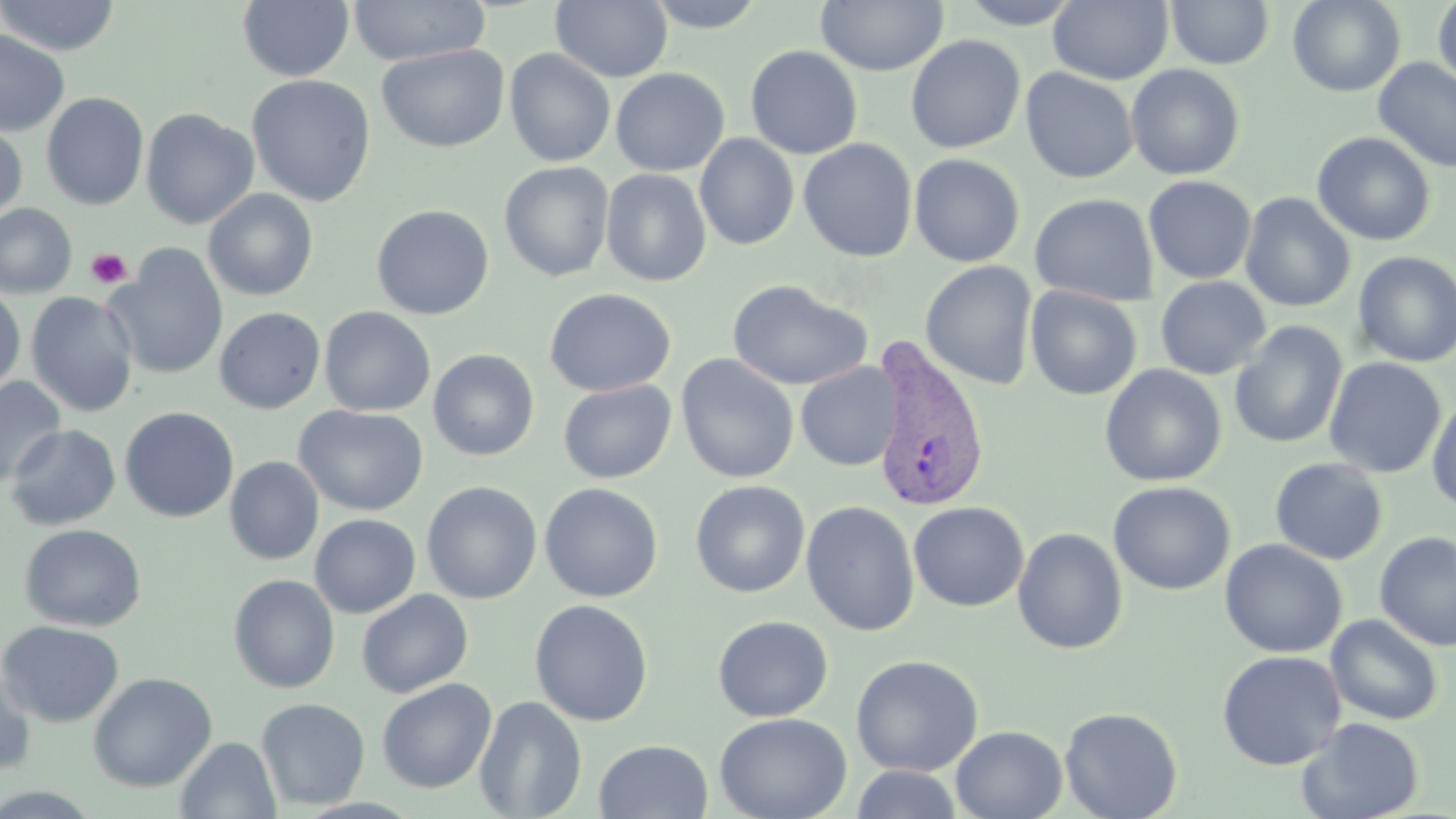

Summary:
  - Coordinate format: approximate bounding boxes as (x1, y1, x2, y2) in pixels
  - Plasmodium vivax-infected red blood cell locations: (868, 338, 991, 515)
  - Uninfected red blood cell locations: (0, 0, 121, 56), (347, 0, 489, 66), (550, 0, 673, 83), (641, 0, 770, 32), (816, 0, 948, 75), (955, 0, 1085, 29), (1048, 0, 1172, 85), (1166, 0, 1275, 69), (1287, 0, 1405, 97), (1432, 0, 1456, 93), (237, 1, 355, 82), (0, 29, 70, 136), (905, 34, 1026, 154), (377, 44, 509, 153), (744, 45, 863, 159), (504, 48, 616, 167), (1373, 58, 1456, 174), (1125, 64, 1245, 181), (1020, 67, 1138, 183), (610, 68, 730, 176), (247, 74, 376, 207), (41, 92, 149, 210), (140, 107, 259, 230), (0, 122, 27, 227), (1311, 131, 1436, 246), (694, 133, 799, 251), (798, 138, 918, 263), (908, 153, 1025, 267), (499, 161, 614, 281), (601, 169, 712, 287), (1143, 175, 1257, 285), (203, 188, 318, 301), (1239, 192, 1356, 312), (1029, 193, 1158, 306), (0, 203, 78, 299), (371, 204, 495, 320), (104, 245, 230, 381), (1352, 250, 1456, 368), (920, 260, 1038, 390), (1155, 276, 1271, 380), (726, 279, 872, 391), (0, 283, 26, 396), (1025, 286, 1142, 400), (544, 288, 676, 397), (26, 291, 138, 417), (701, 301, 829, 471), (214, 306, 326, 414), (319, 306, 436, 416), (1229, 321, 1348, 450), (428, 349, 540, 461), (675, 353, 799, 484), (1323, 357, 1447, 479), (795, 361, 903, 471), (1099, 364, 1227, 487), (0, 376, 66, 487), (558, 379, 676, 483), (1427, 394, 1456, 516), (294, 404, 430, 516), (119, 406, 239, 522), (5, 424, 120, 529), (225, 456, 324, 565), (1269, 457, 1388, 565), (690, 479, 810, 598), (421, 481, 542, 604), (1108, 481, 1235, 595), (539, 482, 663, 603), (801, 500, 920, 636), (908, 501, 1029, 612), (309, 513, 421, 618), (19, 523, 146, 632), (1012, 527, 1128, 654), (1374, 531, 1455, 651), (1220, 538, 1347, 658), (228, 574, 340, 693), (356, 589, 473, 698), (529, 599, 653, 727), (1325, 614, 1444, 726), (712, 615, 834, 722), (0, 620, 124, 727), (1216, 650, 1346, 770), (850, 654, 984, 777), (0, 661, 38, 778), (88, 672, 217, 792), (376, 677, 498, 793), (474, 695, 587, 818), (255, 697, 370, 810), (1059, 706, 1183, 819), (714, 712, 852, 819), (1296, 716, 1425, 819), (950, 725, 1067, 819), (175, 736, 281, 819), (594, 739, 714, 818), (850, 765, 963, 819), (0, 786, 104, 818)
  - Platelet locations: (86, 247, 132, 289)
  - Slide-level diagnosis: Plasmodium vivax
  - Magnification: 1000x
  - Field of view: single
  - Preparation: thin blood film
  - Image size: 1456×819 pixels
  - Stain: May-Grünwald-Giemsa
  - Modality: optical microscopy